Give the position of every Plasmodium parasite.
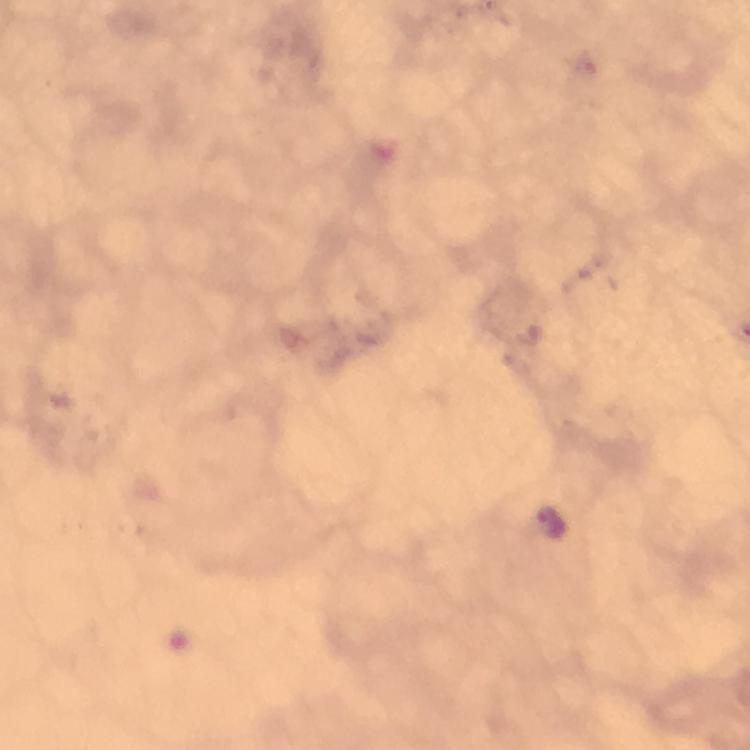
Approximate centers as [x, y] in pixels.
Plasmodium parasites: [552, 521].

{
  "cropped_from": "one field of view",
  "capture": "smartphone mounted on the microscope",
  "preparation": "thick smear",
  "context": "from a malaria diagnostic workup",
  "immersion_oil": "used",
  "image_size": "750×750 pixels",
  "stain": "Giemsa",
  "magnification": "100x"
}